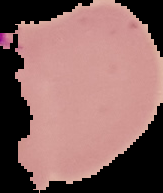

Malaria status: parasitized. Image is 163×193 pixels. Cell region segmented out of the field of view; the surrounding area is masked to black. From a thin blood film.